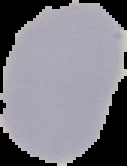
Summary:
  - Result: no Plasmodium parasites seen
  - Image type: segmented cell region on a black background
  - Image size: 127×166 pixels
  - Preparation: thin blood film